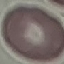
Summary:
  - Result: no malaria parasites detected
  - Stain: Giemsa
  - Image type: automatically extracted cell patch, resized to 64 × 64 pixels
  - Preparation: thin blood smear
  - Capture: smartphone camera at the microscope eyepiece